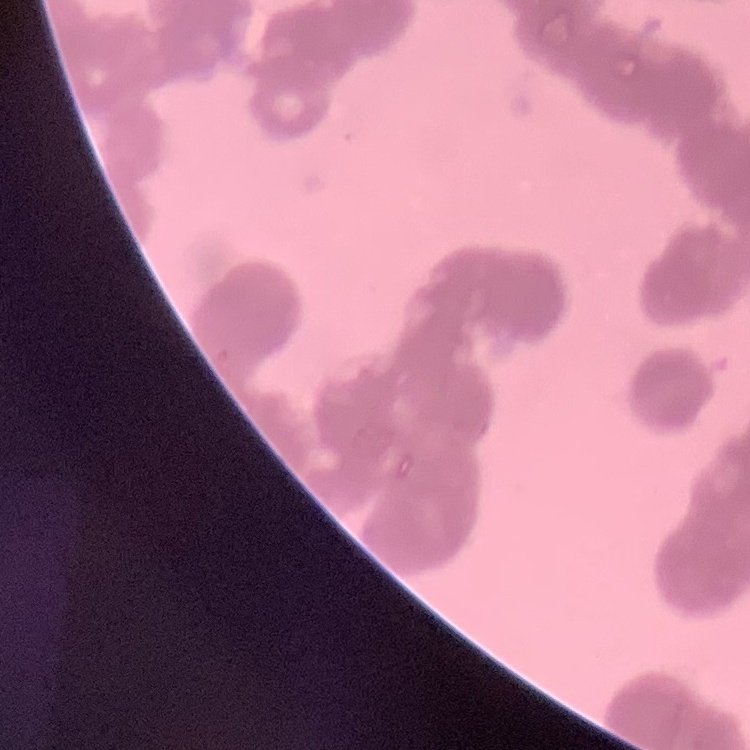
erythrocyte morphology = rouleaux formation
image type = one tile cut from a larger photomicrograph
stain = Field's or Giemsa
preparation = thin peripheral smear